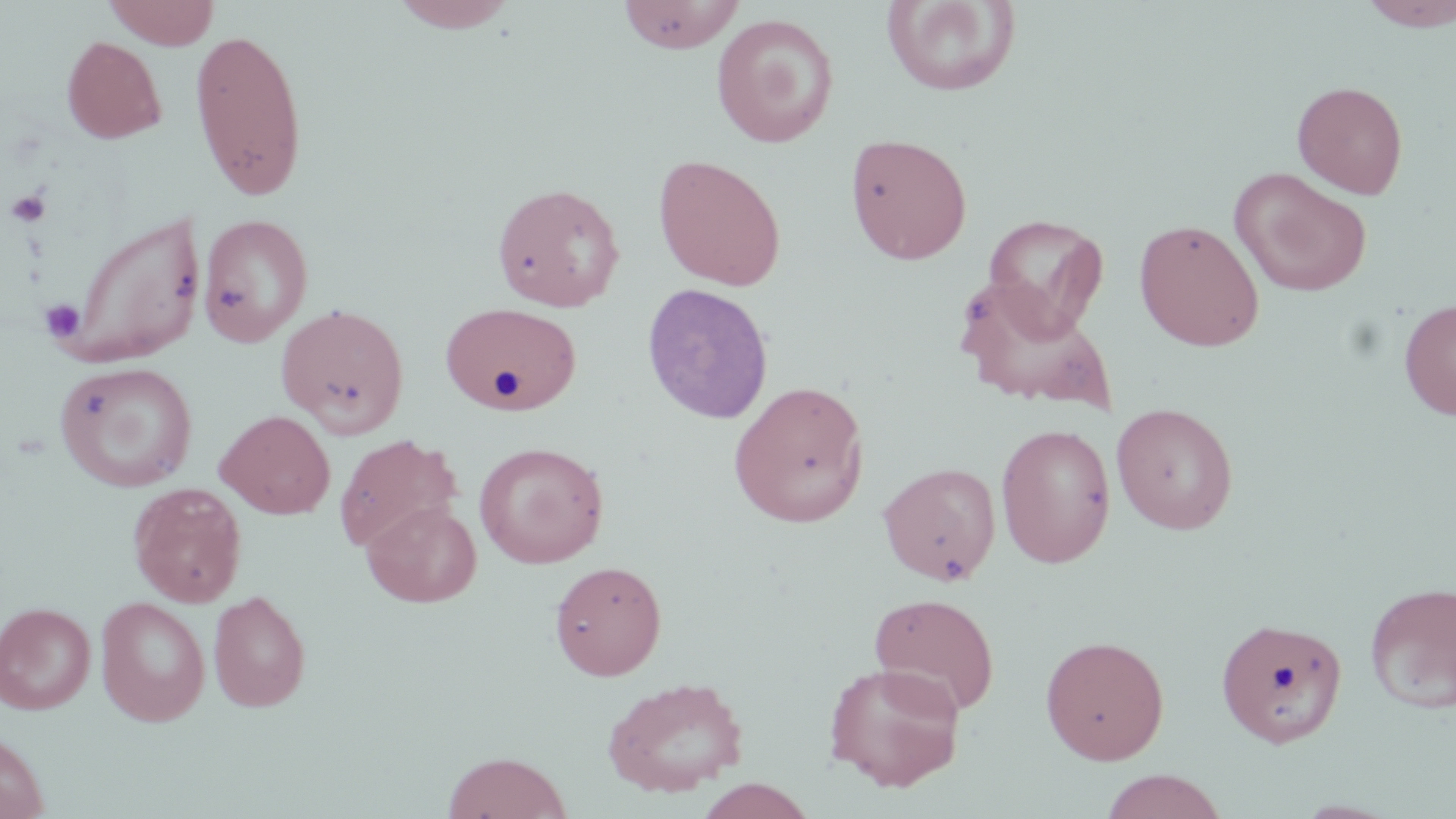
Approximate bounding boxes as named x1/y1/x2/y2 corners in pixels. Uninfected red blood cell locations: (x1=104, y1=0, x2=220, y2=49), (x1=387, y1=0, x2=522, y2=33), (x1=880, y1=0, x2=1022, y2=97), (x1=1357, y1=0, x2=1456, y2=31), (x1=616, y1=1, x2=745, y2=53), (x1=711, y1=13, x2=839, y2=148), (x1=189, y1=26, x2=309, y2=201), (x1=61, y1=35, x2=167, y2=144), (x1=1292, y1=80, x2=1409, y2=198), (x1=845, y1=132, x2=973, y2=265), (x1=653, y1=153, x2=787, y2=291), (x1=1230, y1=168, x2=1372, y2=297), (x1=491, y1=181, x2=626, y2=312), (x1=62, y1=210, x2=206, y2=367), (x1=198, y1=213, x2=314, y2=347), (x1=981, y1=213, x2=1109, y2=337), (x1=1133, y1=218, x2=1266, y2=351), (x1=954, y1=279, x2=1117, y2=412), (x1=641, y1=283, x2=774, y2=424), (x1=1398, y1=297, x2=1456, y2=420), (x1=441, y1=302, x2=582, y2=414), (x1=276, y1=303, x2=410, y2=438), (x1=53, y1=360, x2=198, y2=492), (x1=729, y1=380, x2=869, y2=528), (x1=1111, y1=403, x2=1239, y2=535), (x1=216, y1=409, x2=336, y2=519), (x1=995, y1=423, x2=1116, y2=568), (x1=333, y1=434, x2=461, y2=553), (x1=474, y1=442, x2=609, y2=569), (x1=878, y1=462, x2=1001, y2=585), (x1=128, y1=482, x2=247, y2=607), (x1=362, y1=500, x2=481, y2=607), (x1=550, y1=560, x2=667, y2=680), (x1=1364, y1=581, x2=1456, y2=714), (x1=208, y1=589, x2=312, y2=712), (x1=868, y1=592, x2=1000, y2=716), (x1=95, y1=596, x2=211, y2=727), (x1=0, y1=601, x2=96, y2=714), (x1=1216, y1=617, x2=1348, y2=748), (x1=1040, y1=635, x2=1169, y2=764), (x1=823, y1=661, x2=966, y2=791), (x1=601, y1=675, x2=750, y2=798), (x1=0, y1=731, x2=49, y2=819), (x1=442, y1=751, x2=572, y2=819), (x1=1098, y1=770, x2=1230, y2=819), (x1=695, y1=778, x2=817, y2=819). Platelet locations: (x1=7, y1=188, x2=51, y2=228), (x1=41, y1=299, x2=86, y2=344). Slide-level diagnosis: negative for blood parasites. Image is 1456×819 pixels. Optical microscopy. Captured at 1000x magnification. Thin blood film. Single field of view. May-Grünwald-Giemsa-stained preparation.